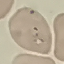

malaria status = parasitized
image type = cell patch, automatically extracted from a larger field of view and resized to 64 × 64 pixels
capture = smartphone camera at the microscope eyepiece
stain = Giemsa
preparation = thin blood film